Report the malaria status of this cell.
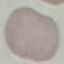
Uninfected.

{
  "image_type": "automatically extracted cell patch, resized to 64 × 64 pixels",
  "capture": "smartphone camera at the microscope eyepiece",
  "stain": "Giemsa",
  "preparation": "thin smear"
}